Describe the morphology of the erythrocytes.
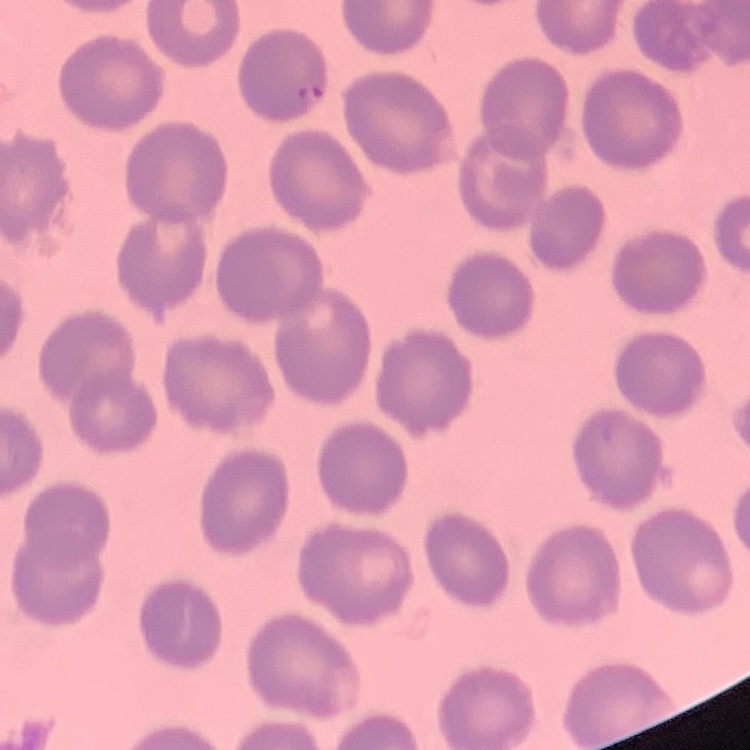
No rouleaux formation.

Thin blood film. One tile cut from a larger photomicrograph. Stained with either Field's or Giemsa.